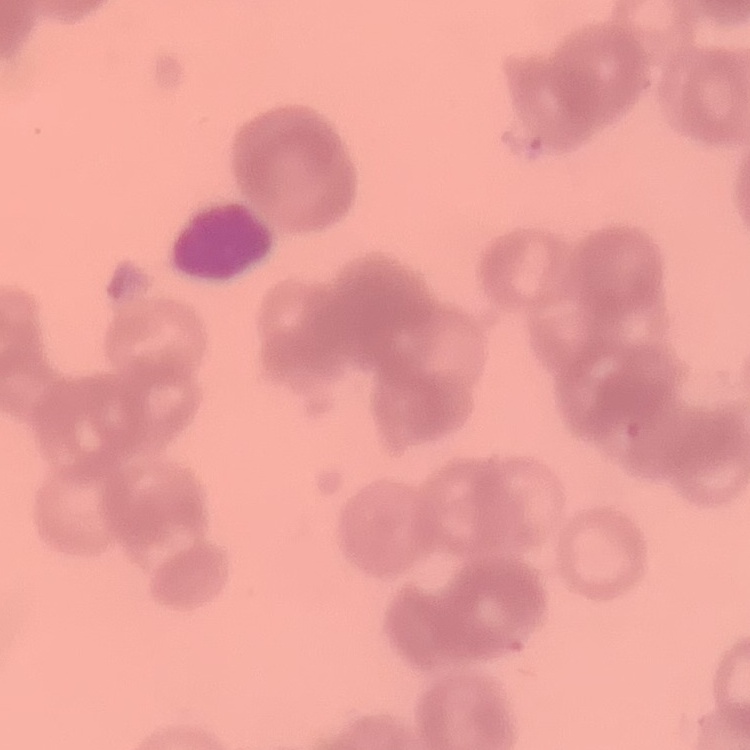

red blood cell morphology = rouleaux formation
preparation = thin blood film
image type = square crop of a larger photomicrograph
stain = Field's or Giemsa